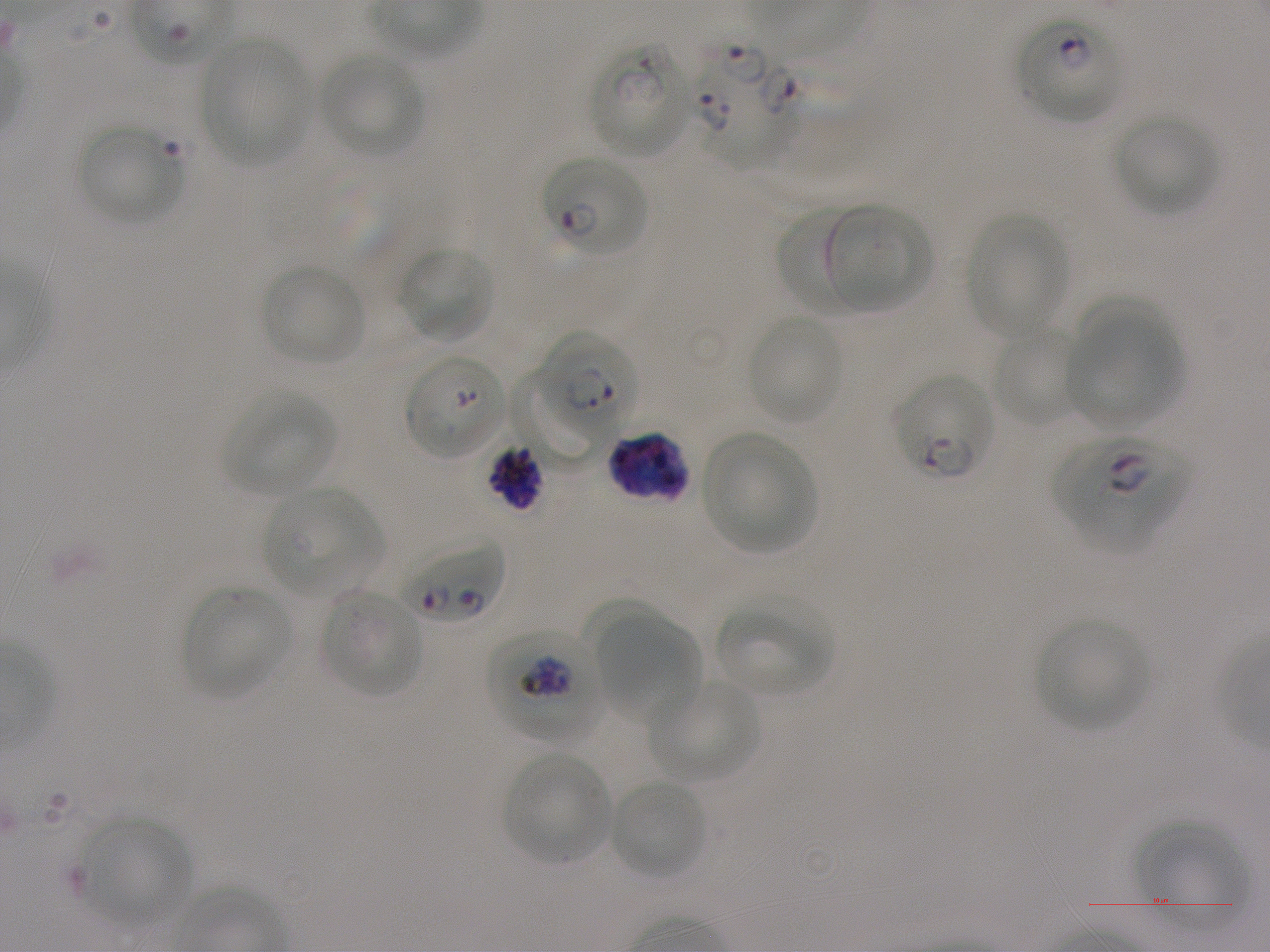
Not every red blood cell is marked. A life-cycle stage — or a range of stages, where the recorded stages span more than one — follows each staged infected red blood cell.
image size = 1270×952 pixels
life-cycle stages observed = ring, trophozoite
objective = 100x, oil immersion, numerical aperture 1.25
locations of infected red blood cells = approximate bounding rectangles given as corner coordinates in pixels from the top-left: (x1=1015, y1=13, x2=1123, y2=124) ring; (x1=588, y1=39, x2=693, y2=158); (x1=689, y1=40, x2=795, y2=166); (x1=541, y1=156, x2=646, y2=256) ring; (x1=538, y1=330, x2=638, y2=434) ring; (x1=509, y1=365, x2=600, y2=472); (x1=894, y1=374, x2=994, y2=479) late ring; (x1=607, y1=430, x2=691, y2=503); (x1=1053, y1=436, x2=1191, y2=548) early ring to early trophozoite; (x1=486, y1=443, x2=542, y2=511); (x1=397, y1=538, x2=504, y2=627); (x1=484, y1=624, x2=604, y2=743) trophozoite
locations of red blood cells of indeterminate infection status = approximate bounding rectangles given as corner coordinates in pixels from the top-left: (x1=405, y1=353, x2=505, y2=459)
locations of uninfected red blood cells = approximate bounding rectangles given as corner coordinates in pixels from the top-left: (x1=199, y1=35, x2=313, y2=167), (x1=320, y1=54, x2=424, y2=158), (x1=1114, y1=114, x2=1218, y2=216), (x1=77, y1=125, x2=182, y2=225), (x1=777, y1=203, x2=869, y2=313), (x1=823, y1=203, x2=932, y2=311), (x1=965, y1=212, x2=1069, y2=337), (x1=398, y1=244, x2=495, y2=344), (x1=261, y1=264, x2=366, y2=366), (x1=1075, y1=297, x2=1170, y2=394), (x1=747, y1=315, x2=844, y2=424), (x1=1070, y1=320, x2=1186, y2=425), (x1=992, y1=329, x2=1084, y2=426), (x1=224, y1=391, x2=337, y2=495), (x1=702, y1=433, x2=816, y2=553), (x1=263, y1=487, x2=381, y2=595), (x1=182, y1=585, x2=290, y2=697), (x1=321, y1=590, x2=423, y2=697), (x1=717, y1=597, x2=834, y2=695), (x1=583, y1=599, x2=665, y2=687), (x1=600, y1=618, x2=699, y2=727), (x1=1035, y1=618, x2=1148, y2=731), (x1=647, y1=680, x2=760, y2=782), (x1=502, y1=752, x2=612, y2=865), (x1=610, y1=778, x2=707, y2=879), (x1=81, y1=818, x2=192, y2=926), (x1=1131, y1=821, x2=1247, y2=930)
culture = in-vitro Plasmodium falciparum strain NF54, static
field of view = one from this slide
preparation = thin blood film
donor blood group = A+
stain = Giemsa